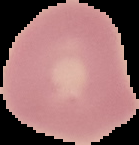

From a thin blood film. Image is 139×145 pixels. Result: negative for Plasmodium parasites. Cell region segmented out of the field of view; the surrounding area is masked to black.